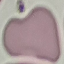

{
  "result": "negative for malaria parasites",
  "preparation": "thin blood smear",
  "capture": "smartphone through the microscope eyepiece",
  "stain": "Giemsa",
  "image_type": "automatically extracted cell patch, resized to 64 × 64 pixels"
}